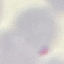
Summary:
  - Malaria status: uninfected
  - Image type: automatically extracted cell patch, resized to 64 × 64 pixels
  - Capture: smartphone camera at the microscope eyepiece
  - Stain: Giemsa
  - Preparation: thin blood film